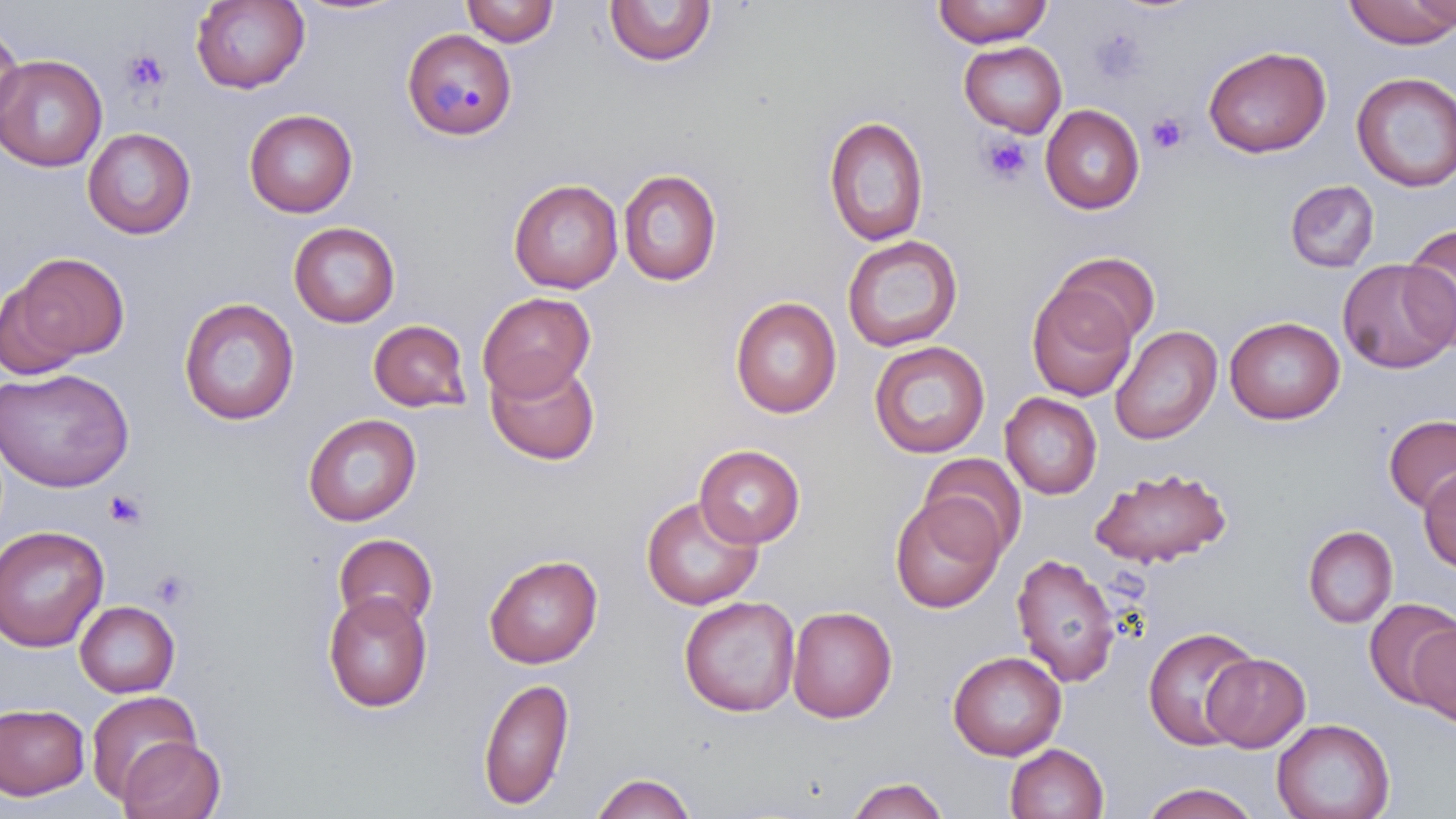

Approximate bounding boxes as named x1/y1/x2/y2 corners in pixels. Platelet locations: (x1=1091, y1=28, x2=1148, y2=84), (x1=122, y1=49, x2=171, y2=95), (x1=1146, y1=112, x2=1189, y2=155), (x1=978, y1=133, x2=1032, y2=187), (x1=104, y1=489, x2=149, y2=531), (x1=151, y1=568, x2=194, y2=610). Plasmodium malariae-infected red blood cell locations: (x1=402, y1=28, x2=516, y2=140). Uninfected red blood cell locations: (x1=191, y1=0, x2=309, y2=93), (x1=932, y1=0, x2=1053, y2=48), (x1=1341, y1=0, x2=1456, y2=48), (x1=1406, y1=0, x2=1456, y2=31), (x1=460, y1=1, x2=560, y2=47), (x1=604, y1=1, x2=717, y2=67), (x1=0, y1=21, x2=24, y2=128), (x1=959, y1=41, x2=1067, y2=137), (x1=1203, y1=45, x2=1331, y2=158), (x1=0, y1=54, x2=107, y2=171), (x1=1351, y1=72, x2=1456, y2=192), (x1=1040, y1=105, x2=1145, y2=214), (x1=244, y1=108, x2=358, y2=217), (x1=823, y1=115, x2=929, y2=247), (x1=82, y1=127, x2=197, y2=240), (x1=618, y1=168, x2=722, y2=286), (x1=508, y1=178, x2=623, y2=293), (x1=1285, y1=180, x2=1380, y2=272), (x1=288, y1=221, x2=400, y2=327), (x1=1400, y1=224, x2=1456, y2=347), (x1=842, y1=234, x2=964, y2=352), (x1=7, y1=251, x2=130, y2=368), (x1=1052, y1=251, x2=1161, y2=347), (x1=1338, y1=259, x2=1456, y2=373), (x1=1026, y1=283, x2=1137, y2=401), (x1=477, y1=292, x2=596, y2=400), (x1=730, y1=296, x2=842, y2=418), (x1=178, y1=297, x2=300, y2=425), (x1=1224, y1=316, x2=1345, y2=424), (x1=368, y1=319, x2=472, y2=412), (x1=1110, y1=324, x2=1223, y2=445), (x1=868, y1=340, x2=990, y2=458), (x1=485, y1=356, x2=601, y2=466), (x1=0, y1=367, x2=134, y2=492), (x1=1000, y1=393, x2=1102, y2=499), (x1=302, y1=413, x2=421, y2=526), (x1=1383, y1=415, x2=1456, y2=514), (x1=694, y1=445, x2=806, y2=548), (x1=920, y1=452, x2=1027, y2=559), (x1=1418, y1=465, x2=1456, y2=573), (x1=1090, y1=466, x2=1232, y2=568), (x1=640, y1=494, x2=763, y2=610), (x1=890, y1=495, x2=1005, y2=612), (x1=1302, y1=524, x2=1397, y2=629), (x1=0, y1=525, x2=109, y2=652), (x1=333, y1=533, x2=438, y2=632), (x1=484, y1=553, x2=603, y2=668), (x1=1011, y1=553, x2=1122, y2=687), (x1=322, y1=591, x2=432, y2=712), (x1=679, y1=595, x2=800, y2=717), (x1=1362, y1=598, x2=1454, y2=706), (x1=74, y1=600, x2=180, y2=698), (x1=787, y1=605, x2=897, y2=723), (x1=1409, y1=623, x2=1456, y2=726), (x1=1143, y1=627, x2=1260, y2=749), (x1=947, y1=650, x2=1067, y2=760), (x1=1203, y1=652, x2=1310, y2=752), (x1=477, y1=676, x2=575, y2=811), (x1=85, y1=691, x2=200, y2=803), (x1=0, y1=703, x2=90, y2=800), (x1=1272, y1=718, x2=1395, y2=819), (x1=117, y1=736, x2=225, y2=819), (x1=1005, y1=743, x2=1109, y2=819), (x1=589, y1=772, x2=698, y2=818), (x1=844, y1=776, x2=952, y2=818), (x1=1138, y1=782, x2=1260, y2=819). Slide-level diagnosis: Plasmodium malariae. Light microscopy. Thin blood film. Image is 1456×819 pixels. May-Grünwald-Giemsa stain. Single field of view. Captured at 1000x magnification.